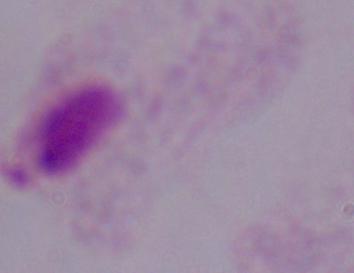
magnification = 1000x
identification = trichomonad
modality = micrograph